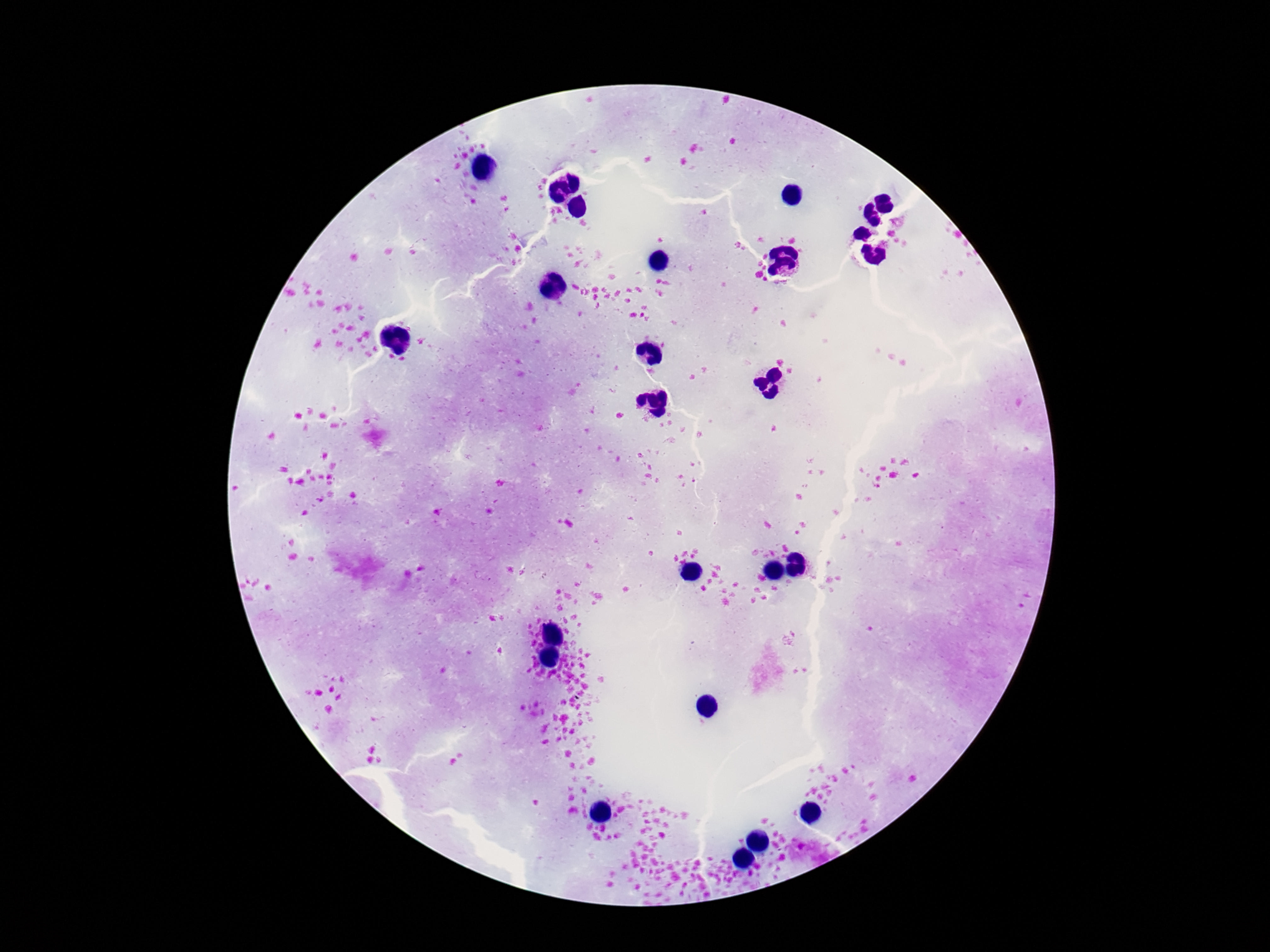

Approximate centers as (x, y) in pixels.
Summary:
  - Leukocyte locations: (531, 90), (513, 113), (457, 137), (667, 141), (564, 246), (723, 295), (720, 316), (499, 379), (587, 379), (475, 387), (611, 552), (499, 567), (620, 597), (879, 614), (721, 663), (485, 688), (608, 691), (403, 705), (403, 737), (692, 742), (387, 744), (478, 751), (704, 765), (788, 788)
  - Preparation: thick peripheral-blood smear
  - Stain: Giemsa
  - Image size: 1270×952 pixels
  - Patient malaria status: negative
  - Capture: smartphone camera through the microscope eyepiece
  - Magnification: 100x
  - Field of view: single